Locate every malaria parasite.
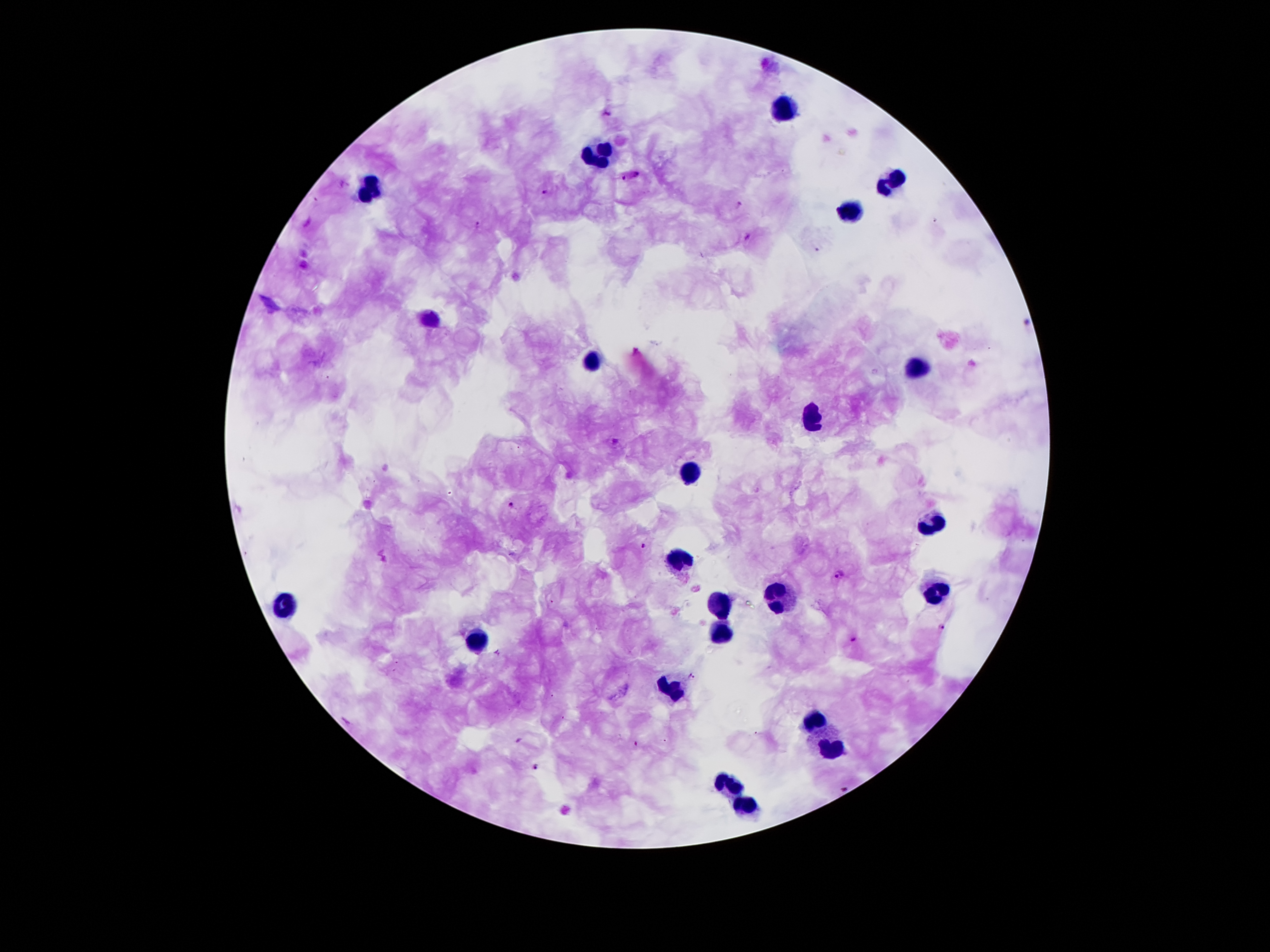

Approximate centers as [x, y] in pixels.
Malaria parasites: [608, 113], [631, 175], [544, 193], [740, 206], [477, 223], [746, 237], [615, 442], [511, 504], [644, 546], [840, 574], [940, 628], [853, 639], [692, 676], [635, 744], [534, 765].

Summary:
  - Leukocyte locations: [783, 106], [595, 153], [892, 181], [371, 192], [851, 209], [431, 319], [589, 360], [922, 364], [815, 418], [690, 474], [933, 524], [681, 557], [937, 590], [774, 594], [718, 602], [283, 603], [716, 634], [477, 643], [673, 690], [813, 717], [834, 749], [731, 784], [742, 805]
  - Field of view: one from this slide
  - Capture: smartphone camera through the microscope eyepiece
  - Patient malaria status: infected with Plasmodium falciparum
  - Stain: Giemsa
  - Image size: 1270×952 pixels
  - Preparation: thick blood film
  - Magnification: 100x